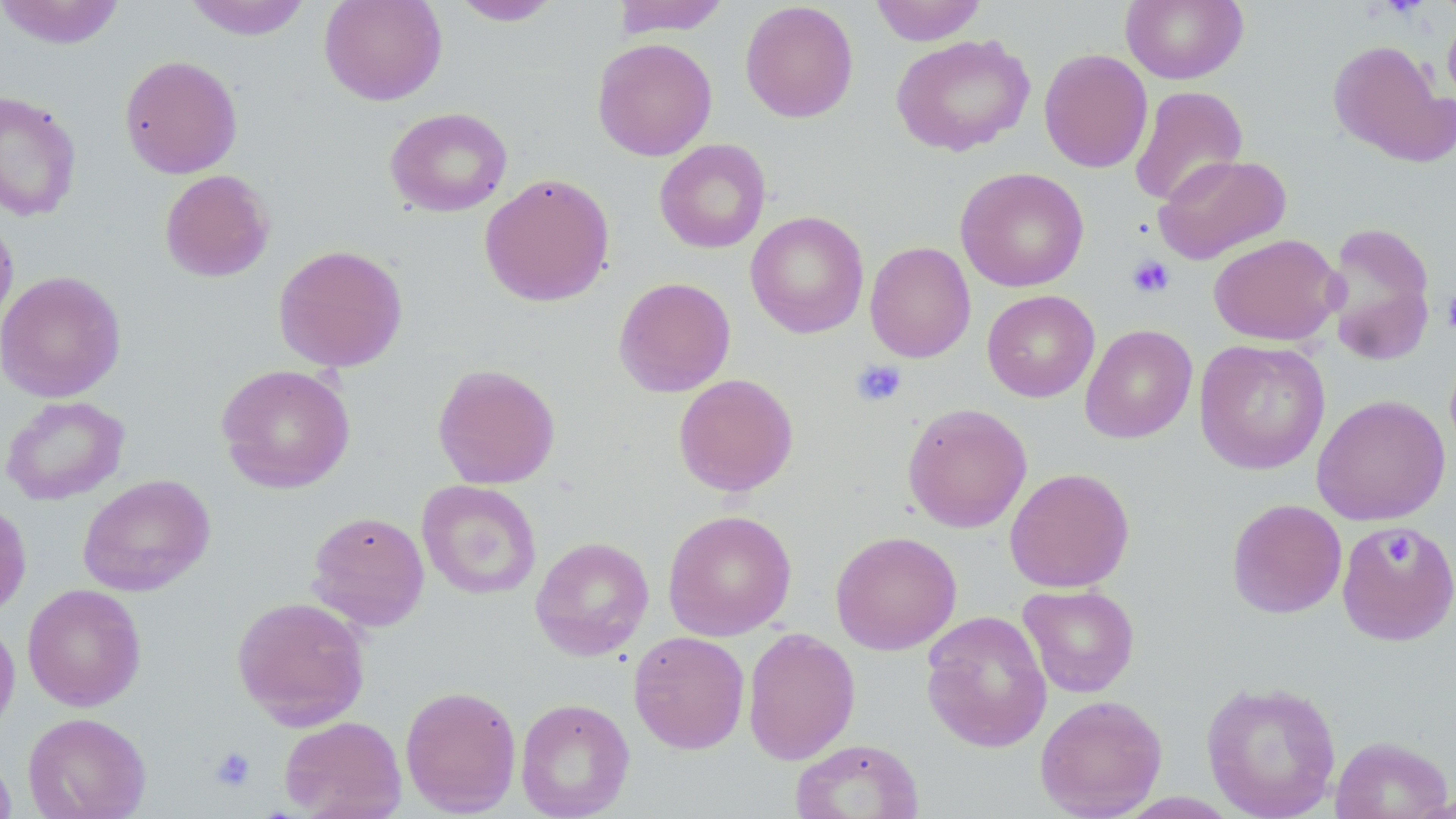

slide-level diagnosis = negative for blood parasites
field of view = one of a larger specimen
image size = 1456×819 pixels
stain = May-Grünwald-Giemsa
platelet locations = approximate bounding boxes as (x1,y1)-(x2,y2) corner pairs in pixels: (1127,255)-(1175,299), (1442,289)-(1456,335), (850,359)-(907,408), (1382,533)-(1416,566), (210,746)-(256,792)
uninfected red blood cell locations = approximate bounding boxes as (x1,y1)-(x2,y2) corner pairs in pixels: (0,0)-(126,49), (184,0)-(312,40), (319,0)-(447,106), (612,0)-(731,37), (869,0)-(987,45), (1121,0)-(1248,85), (450,1)-(564,26), (739,2)-(859,123), (1442,12)-(1456,111), (891,34)-(1035,157), (592,38)-(718,161), (1328,39)-(1455,167), (1039,49)-(1153,173), (119,55)-(243,179), (1129,86)-(1249,207), (0,90)-(82,222), (385,107)-(513,217), (654,139)-(771,254), (1153,153)-(1291,264), (955,167)-(1089,292), (160,169)-(274,282), (479,172)-(615,307), (0,211)-(18,337), (745,211)-(869,339), (1321,221)-(1437,362), (1209,233)-(1342,346), (864,241)-(976,363), (273,244)-(409,372), (0,270)-(126,402), (613,277)-(736,397), (982,290)-(1099,402), (1080,323)-(1198,444), (1194,339)-(1330,475), (216,363)-(356,494), (432,363)-(561,489), (673,373)-(798,497), (1312,394)-(1451,525), (1,395)-(129,506), (903,402)-(1032,533), (1004,467)-(1135,592), (78,474)-(216,596), (417,479)-(542,600), (0,499)-(32,620), (1226,499)-(1347,618), (662,509)-(797,641), (306,511)-(430,632), (1337,520)-(1455,646), (830,530)-(962,655), (530,536)-(654,661), (23,584)-(146,711), (1018,584)-(1140,698), (232,595)-(371,730), (921,610)-(1052,753), (0,616)-(20,738), (742,628)-(860,765), (629,631)-(750,754), (1202,678)-(1342,819), (400,684)-(522,816), (1035,694)-(1167,818), (515,697)-(635,819), (23,712)-(151,819), (279,715)-(407,819), (1329,735)-(1452,819), (790,738)-(924,819), (0,748)-(16,819)
modality = light microscopy
magnification = 1000x
preparation = thin blood film